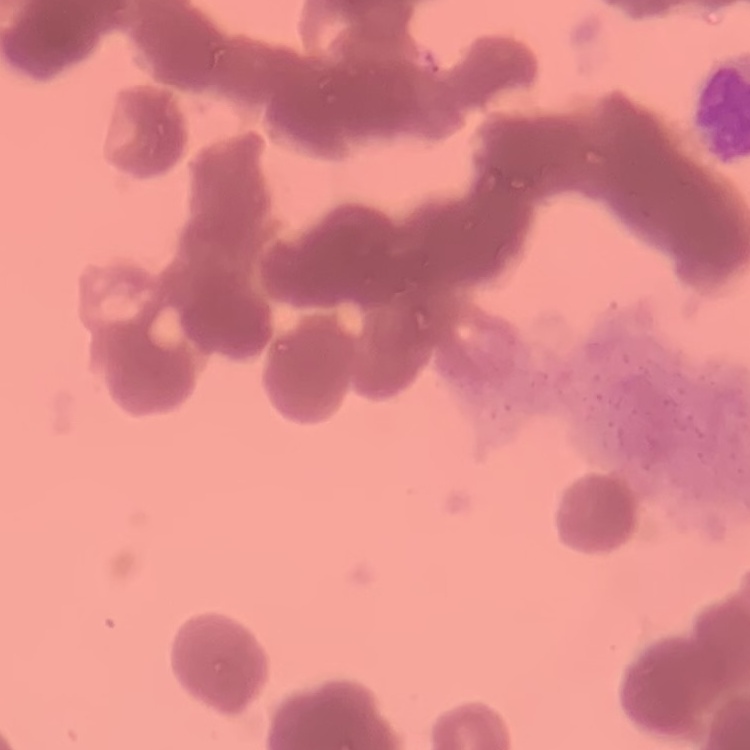

The red blood cells show rouleaux formation. Square crop of a larger photomicrograph. Thin blood film. Stained with either Field's or Giemsa.